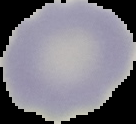

Image is 136×124 pixels. Malaria status: uninfected. The area outside the segmented cell region is set to black. From a thin blood smear.